State which parasite is depicted.
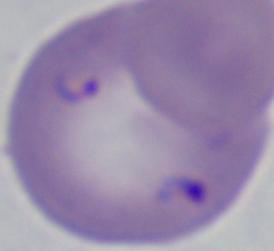
This is Babesia.

Captured at 1000x magnification. Photomicrograph.